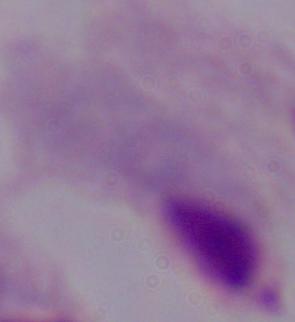
Summary:
  - Identification: trichomonad
  - Magnification: 1000x
  - Modality: micrograph